Report the malaria status of this cell.
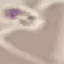

Uninfected.

Summary:
  - Capture: smartphone camera at the microscope eyepiece
  - Stain: Giemsa
  - Preparation: thin smear
  - Image type: cell patch, automatically extracted from a larger field of view and resized to 64 × 64 pixels